Assess this cell for malaria.
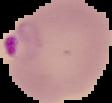
Parasitized.

image type = segmented cell region with the area outside set to black
image size = 112×103 pixels
preparation = thin blood smear